Evaluate for parasitized red blood cells.
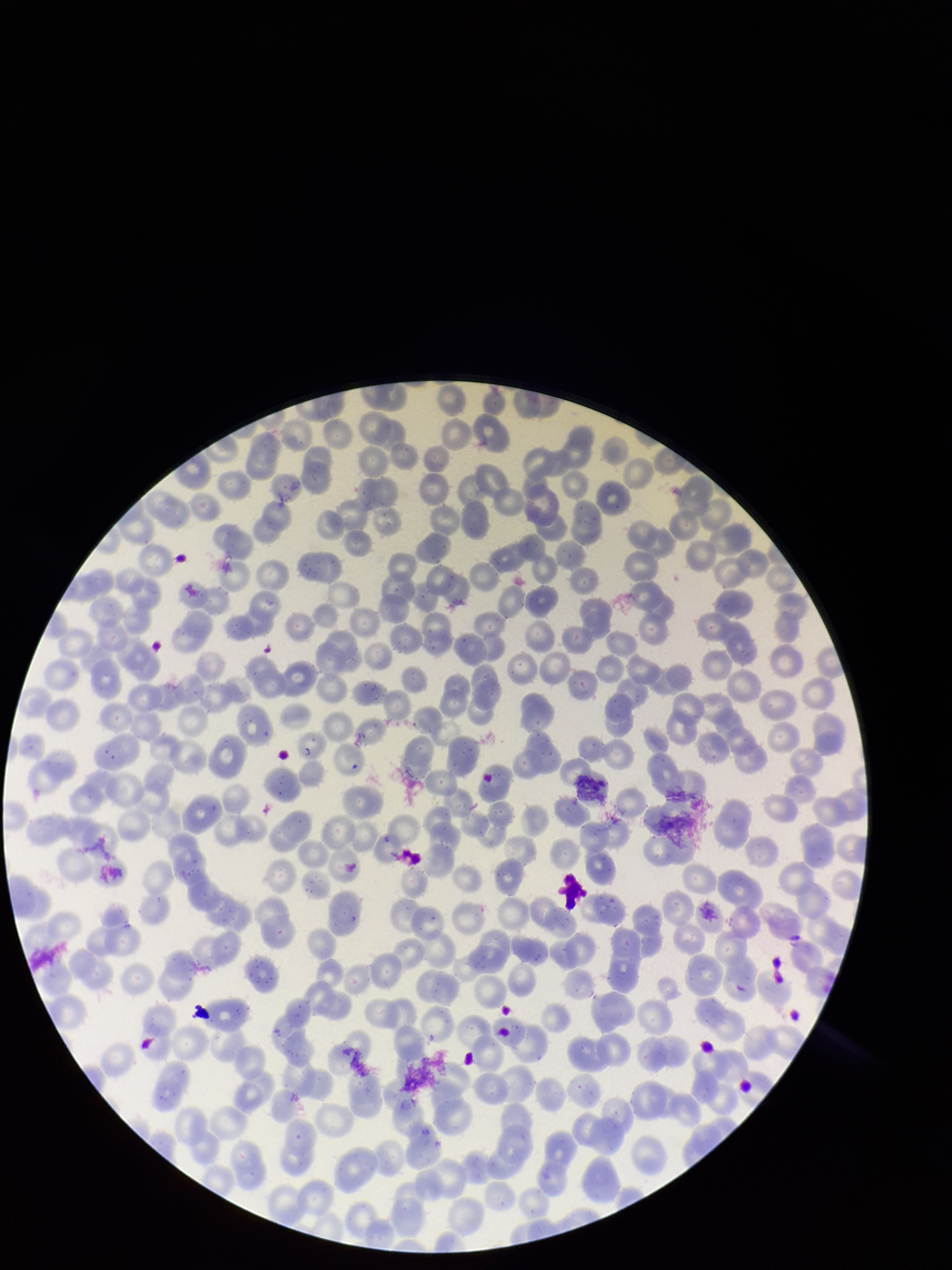
None identified.

Patient malaria status: positive. Species reported for this patient: Plasmodium vivax. Image is 952×1270 pixels. Parasitized red blood cell count: 0. Giemsa stain. Preparation: thin. Photographed through the microscope eyepiece with a smartphone camera. One field from this slide. Red blood cell count: 221.